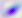
Photomicrograph. Toxoplasma gondii is seen. 400x magnification.